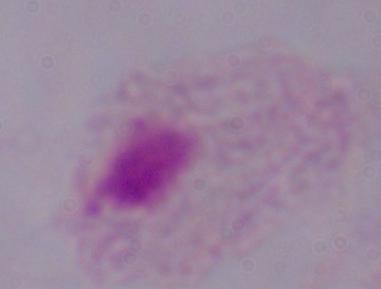

modality = photomicrograph
magnification = 1000x
identification = trichomonad